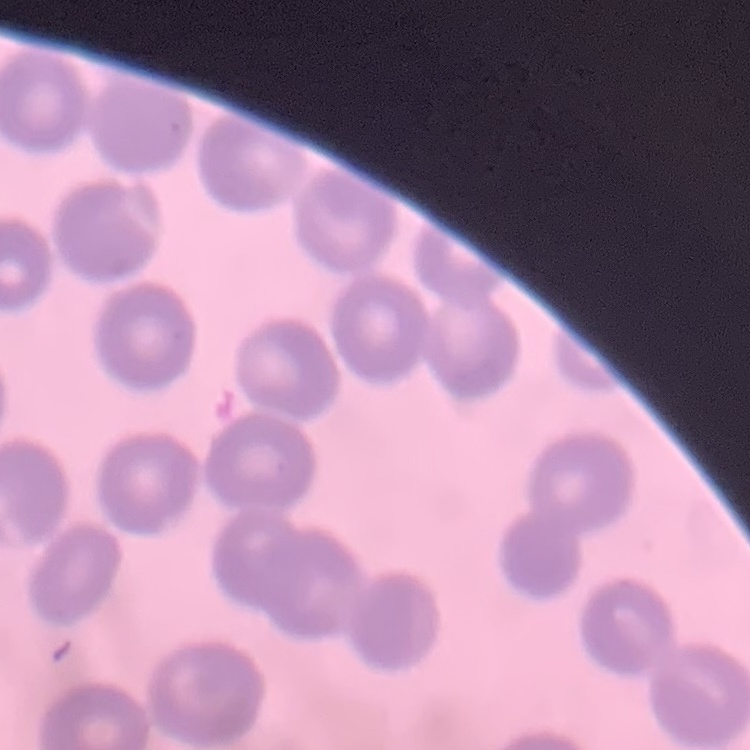

The red blood cells exhibit no rouleaux formation. Thin blood film. Square crop of a larger photomicrograph. Field's or Giemsa stain.